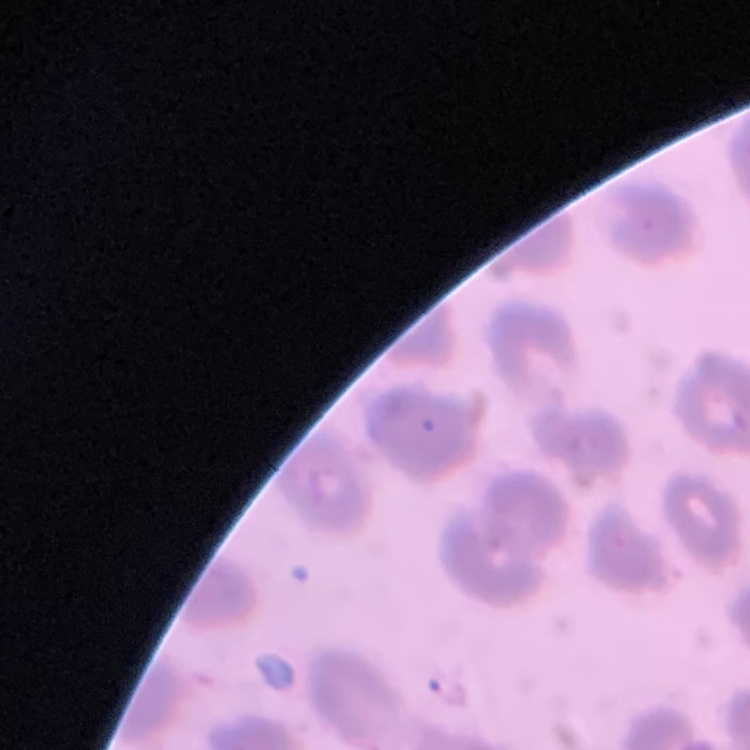

Summary:
  - Erythrocyte morphology: no rouleaux formation
  - Stain: Field's or Giemsa
  - Preparation: thin blood film
  - Image type: square crop of a larger photomicrograph